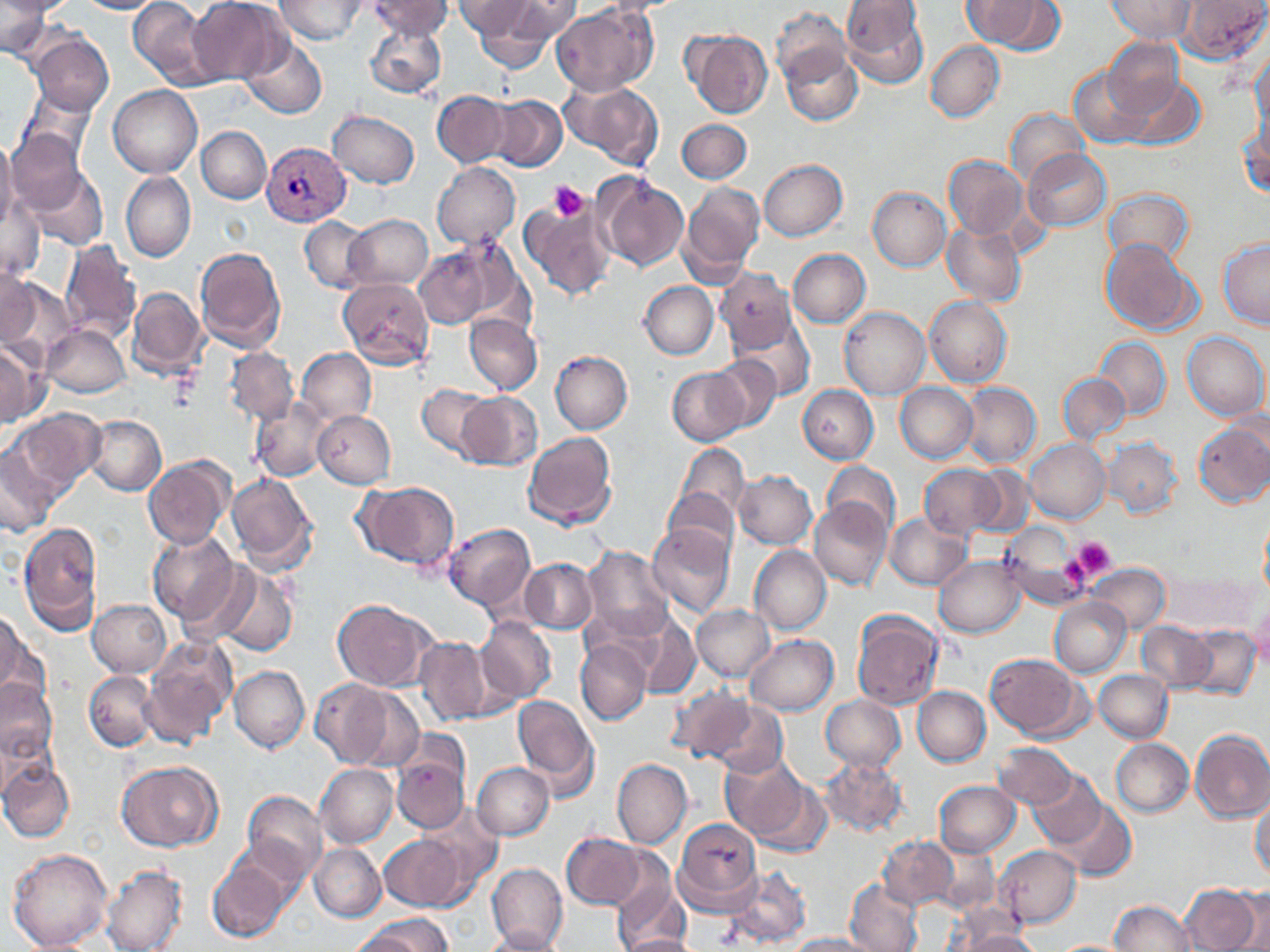
Approximate bounding boxes as named x1/y1/x2/y2 corners in pixels. Platelet locations: (x1=548, y1=182, x2=590, y2=221), (x1=1070, y1=537, x2=1116, y2=582). Uninfected red blood cell locations: (x1=0, y1=0, x2=52, y2=60), (x1=0, y1=0, x2=75, y2=17), (x1=77, y1=0, x2=162, y2=14), (x1=128, y1=0, x2=214, y2=88), (x1=188, y1=0, x2=287, y2=84), (x1=276, y1=0, x2=368, y2=43), (x1=368, y1=0, x2=452, y2=40), (x1=453, y1=0, x2=537, y2=40), (x1=500, y1=0, x2=582, y2=42), (x1=594, y1=0, x2=688, y2=15), (x1=962, y1=0, x2=1055, y2=49), (x1=1105, y1=0, x2=1195, y2=43), (x1=1176, y1=0, x2=1268, y2=64), (x1=841, y1=1, x2=929, y2=87), (x1=472, y1=5, x2=561, y2=68), (x1=552, y1=6, x2=656, y2=96), (x1=771, y1=7, x2=851, y2=83), (x1=365, y1=21, x2=447, y2=100), (x1=684, y1=30, x2=772, y2=119), (x1=28, y1=32, x2=113, y2=115), (x1=240, y1=35, x2=328, y2=119), (x1=1103, y1=38, x2=1186, y2=119), (x1=925, y1=41, x2=1004, y2=122), (x1=780, y1=47, x2=862, y2=125), (x1=1250, y1=53, x2=1269, y2=135), (x1=1068, y1=66, x2=1151, y2=148), (x1=1121, y1=73, x2=1204, y2=147), (x1=564, y1=82, x2=663, y2=168), (x1=109, y1=85, x2=202, y2=178), (x1=20, y1=89, x2=97, y2=163), (x1=433, y1=91, x2=511, y2=168), (x1=490, y1=94, x2=567, y2=171), (x1=1005, y1=108, x2=1088, y2=187), (x1=327, y1=111, x2=420, y2=188), (x1=677, y1=119, x2=751, y2=184), (x1=1239, y1=122, x2=1269, y2=200), (x1=196, y1=127, x2=271, y2=203), (x1=4, y1=129, x2=87, y2=215), (x1=0, y1=137, x2=19, y2=232), (x1=1022, y1=149, x2=1110, y2=230), (x1=944, y1=155, x2=1027, y2=240), (x1=758, y1=159, x2=847, y2=241), (x1=432, y1=162, x2=520, y2=249), (x1=23, y1=167, x2=108, y2=252), (x1=121, y1=171, x2=196, y2=263), (x1=596, y1=172, x2=689, y2=271), (x1=680, y1=180, x2=765, y2=281), (x1=868, y1=186, x2=951, y2=270), (x1=1104, y1=187, x2=1194, y2=266), (x1=2, y1=195, x2=44, y2=280), (x1=518, y1=195, x2=616, y2=302), (x1=344, y1=214, x2=432, y2=288), (x1=300, y1=216, x2=371, y2=292), (x1=942, y1=223, x2=1026, y2=305), (x1=442, y1=237, x2=533, y2=332), (x1=1101, y1=238, x2=1200, y2=337), (x1=1218, y1=238, x2=1270, y2=329), (x1=60, y1=241, x2=141, y2=342), (x1=415, y1=244, x2=496, y2=328), (x1=194, y1=246, x2=286, y2=352), (x1=787, y1=249, x2=871, y2=327), (x1=717, y1=263, x2=870, y2=341), (x1=0, y1=269, x2=44, y2=350), (x1=717, y1=270, x2=798, y2=352), (x1=339, y1=277, x2=433, y2=370), (x1=5, y1=281, x2=75, y2=369), (x1=639, y1=282, x2=718, y2=359), (x1=128, y1=287, x2=207, y2=378), (x1=925, y1=296, x2=1013, y2=387), (x1=839, y1=307, x2=930, y2=400), (x1=463, y1=313, x2=542, y2=394), (x1=733, y1=313, x2=817, y2=401), (x1=42, y1=325, x2=130, y2=397), (x1=1183, y1=331, x2=1269, y2=421), (x1=1094, y1=337, x2=1172, y2=420), (x1=0, y1=342, x2=45, y2=428), (x1=225, y1=347, x2=298, y2=423), (x1=296, y1=348, x2=377, y2=424), (x1=551, y1=351, x2=633, y2=433), (x1=708, y1=356, x2=782, y2=433), (x1=667, y1=367, x2=747, y2=445), (x1=1058, y1=373, x2=1131, y2=444), (x1=895, y1=382, x2=978, y2=463), (x1=960, y1=382, x2=1040, y2=468), (x1=417, y1=384, x2=494, y2=458), (x1=797, y1=385, x2=878, y2=463), (x1=456, y1=392, x2=543, y2=470), (x1=250, y1=397, x2=331, y2=482), (x1=9, y1=408, x2=104, y2=491), (x1=312, y1=411, x2=395, y2=487), (x1=82, y1=415, x2=166, y2=496), (x1=1194, y1=421, x2=1270, y2=507), (x1=522, y1=431, x2=617, y2=529), (x1=1104, y1=438, x2=1183, y2=518), (x1=1025, y1=439, x2=1110, y2=523), (x1=674, y1=443, x2=750, y2=522), (x1=1, y1=444, x2=61, y2=536), (x1=144, y1=457, x2=233, y2=550), (x1=821, y1=462, x2=899, y2=535), (x1=918, y1=464, x2=1004, y2=539), (x1=969, y1=465, x2=1035, y2=538), (x1=734, y1=471, x2=817, y2=549), (x1=225, y1=472, x2=318, y2=572), (x1=353, y1=480, x2=460, y2=574), (x1=663, y1=487, x2=740, y2=558), (x1=809, y1=497, x2=893, y2=591), (x1=884, y1=514, x2=972, y2=589), (x1=1259, y1=515, x2=1269, y2=599), (x1=18, y1=522, x2=103, y2=634), (x1=443, y1=524, x2=535, y2=610), (x1=647, y1=524, x2=735, y2=618), (x1=998, y1=524, x2=1089, y2=609), (x1=148, y1=531, x2=240, y2=623), (x1=749, y1=546, x2=830, y2=635), (x1=582, y1=547, x2=675, y2=642), (x1=933, y1=556, x2=1026, y2=638), (x1=520, y1=558, x2=597, y2=634), (x1=1086, y1=563, x2=1169, y2=635), (x1=211, y1=566, x2=298, y2=658), (x1=1164, y1=569, x2=1257, y2=635), (x1=1049, y1=597, x2=1131, y2=677), (x1=88, y1=600, x2=171, y2=677), (x1=333, y1=600, x2=437, y2=692), (x1=1249, y1=602, x2=1270, y2=671), (x1=692, y1=605, x2=775, y2=680), (x1=0, y1=610, x2=24, y2=697), (x1=852, y1=611, x2=943, y2=710), (x1=632, y1=615, x2=701, y2=700), (x1=475, y1=617, x2=557, y2=704), (x1=1137, y1=621, x2=1217, y2=691), (x1=1184, y1=625, x2=1261, y2=700), (x1=744, y1=634, x2=838, y2=716), (x1=415, y1=636, x2=490, y2=725), (x1=143, y1=637, x2=234, y2=747), (x1=574, y1=638, x2=652, y2=726), (x1=984, y1=654, x2=1084, y2=740), (x1=230, y1=666, x2=310, y2=753), (x1=1094, y1=670, x2=1174, y2=743), (x1=84, y1=671, x2=159, y2=750), (x1=0, y1=678, x2=57, y2=764), (x1=309, y1=679, x2=396, y2=769), (x1=666, y1=683, x2=755, y2=764), (x1=912, y1=686, x2=990, y2=766), (x1=346, y1=689, x2=426, y2=771), (x1=512, y1=695, x2=598, y2=794), (x1=819, y1=695, x2=906, y2=773), (x1=708, y1=698, x2=788, y2=778), (x1=1190, y1=728, x2=1270, y2=823), (x1=392, y1=729, x2=472, y2=803), (x1=1111, y1=738, x2=1194, y2=816), (x1=992, y1=743, x2=1078, y2=809), (x1=392, y1=756, x2=468, y2=832), (x1=719, y1=756, x2=809, y2=840), (x1=820, y1=758, x2=908, y2=836), (x1=612, y1=759, x2=691, y2=849), (x1=1, y1=760, x2=74, y2=843), (x1=115, y1=760, x2=222, y2=851), (x1=314, y1=763, x2=398, y2=847), (x1=472, y1=763, x2=554, y2=840), (x1=1029, y1=772, x2=1105, y2=846), (x1=1026, y1=773, x2=1118, y2=914), (x1=749, y1=778, x2=833, y2=859), (x1=934, y1=781, x2=1021, y2=856), (x1=241, y1=790, x2=327, y2=880), (x1=1250, y1=794, x2=1270, y2=882), (x1=1056, y1=801, x2=1136, y2=881), (x1=417, y1=805, x2=502, y2=889), (x1=674, y1=819, x2=762, y2=914), (x1=562, y1=832, x2=645, y2=910), (x1=379, y1=834, x2=468, y2=910), (x1=878, y1=836, x2=958, y2=911), (x1=928, y1=843, x2=1000, y2=914), (x1=309, y1=844, x2=386, y2=922), (x1=994, y1=845, x2=1082, y2=928), (x1=8, y1=848, x2=111, y2=951), (x1=208, y1=857, x2=291, y2=942), (x1=487, y1=863, x2=568, y2=952), (x1=725, y1=863, x2=812, y2=948), (x1=100, y1=865, x2=188, y2=952), (x1=611, y1=872, x2=690, y2=952), (x1=846, y1=880, x2=922, y2=952), (x1=1181, y1=883, x2=1262, y2=951), (x1=1224, y1=888, x2=1270, y2=950), (x1=1109, y1=901, x2=1196, y2=952), (x1=366, y1=913, x2=452, y2=951), (x1=947, y1=913, x2=1033, y2=949), (x1=346, y1=926, x2=428, y2=952), (x1=479, y1=928, x2=567, y2=951), (x1=954, y1=930, x2=1042, y2=952), (x1=785, y1=933, x2=877, y2=952), (x1=619, y1=934, x2=701, y2=952), (x1=1053, y1=939, x2=1133, y2=951). Plasmodium vivax-infected red blood cell locations: (x1=262, y1=142, x2=351, y2=226). Slide-level diagnosis: Plasmodium vivax. 1000x magnification. May-Grünwald-Giemsa stain. Single field of view. Light microscopy. Image is 1270×952 pixels. Thin blood smear.